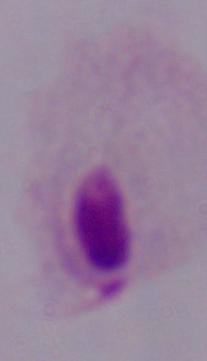 Captured at 1000x magnification. A trichomonad is seen. Micrograph.